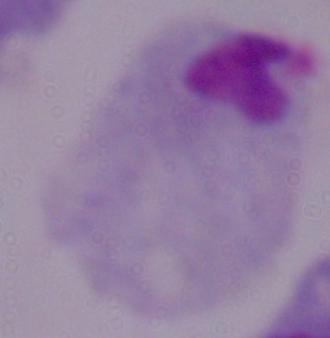
Summary:
  - Modality: micrograph
  - Magnification: 1000x
  - Identification: trichomonad